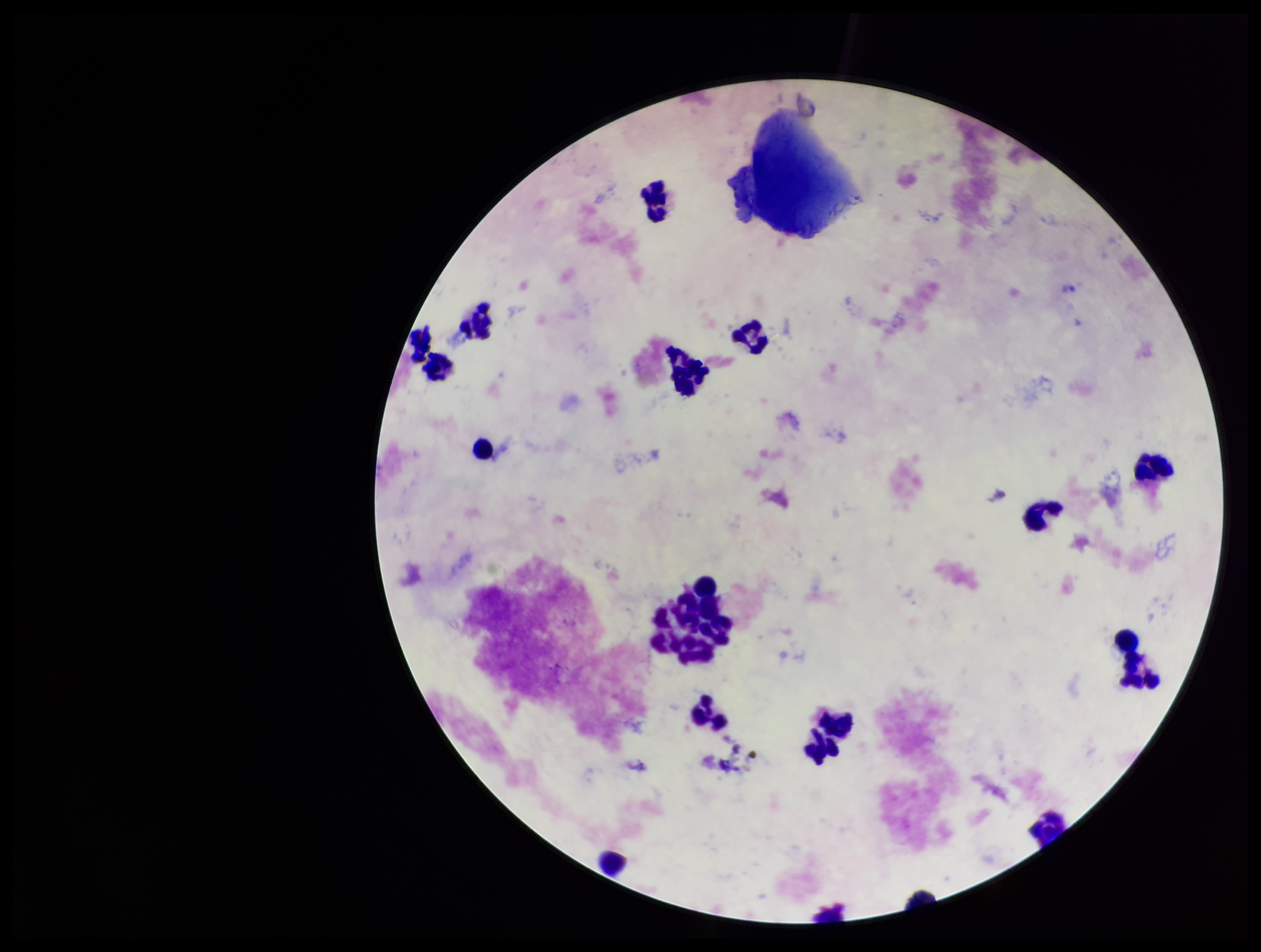

Leukocyte count: 20. Parasite count: 0. Image is 1261×952 pixels. Patient malaria status: negative. Preparation: thick blood smear. Stained with Giemsa. One field from this slide. Plasmodium parasites: none seen. Smartphone photograph taken through the eyepiece of a microscope.